Identify the cell.
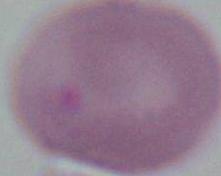

An erythrocyte.

Summary:
  - Magnification: 1000x
  - Modality: photomicrograph